Describe the morphology of the erythrocytes.
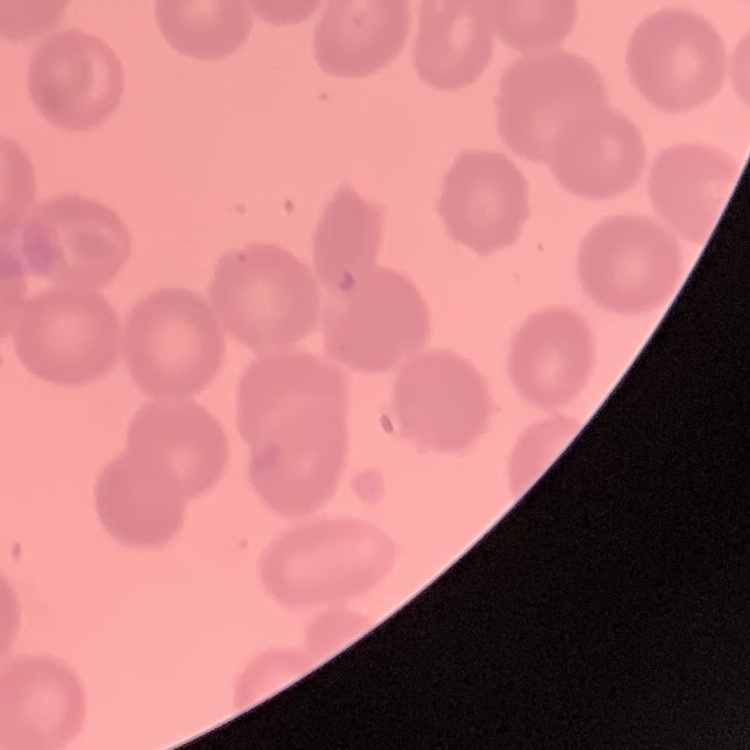

They show no rouleaux formation.

Summary:
  - Preparation: thin blood smear
  - Stain: Field's or Giemsa
  - Image type: one tile cut from a larger photomicrograph